Give the extent of all uninfected red blood cells.
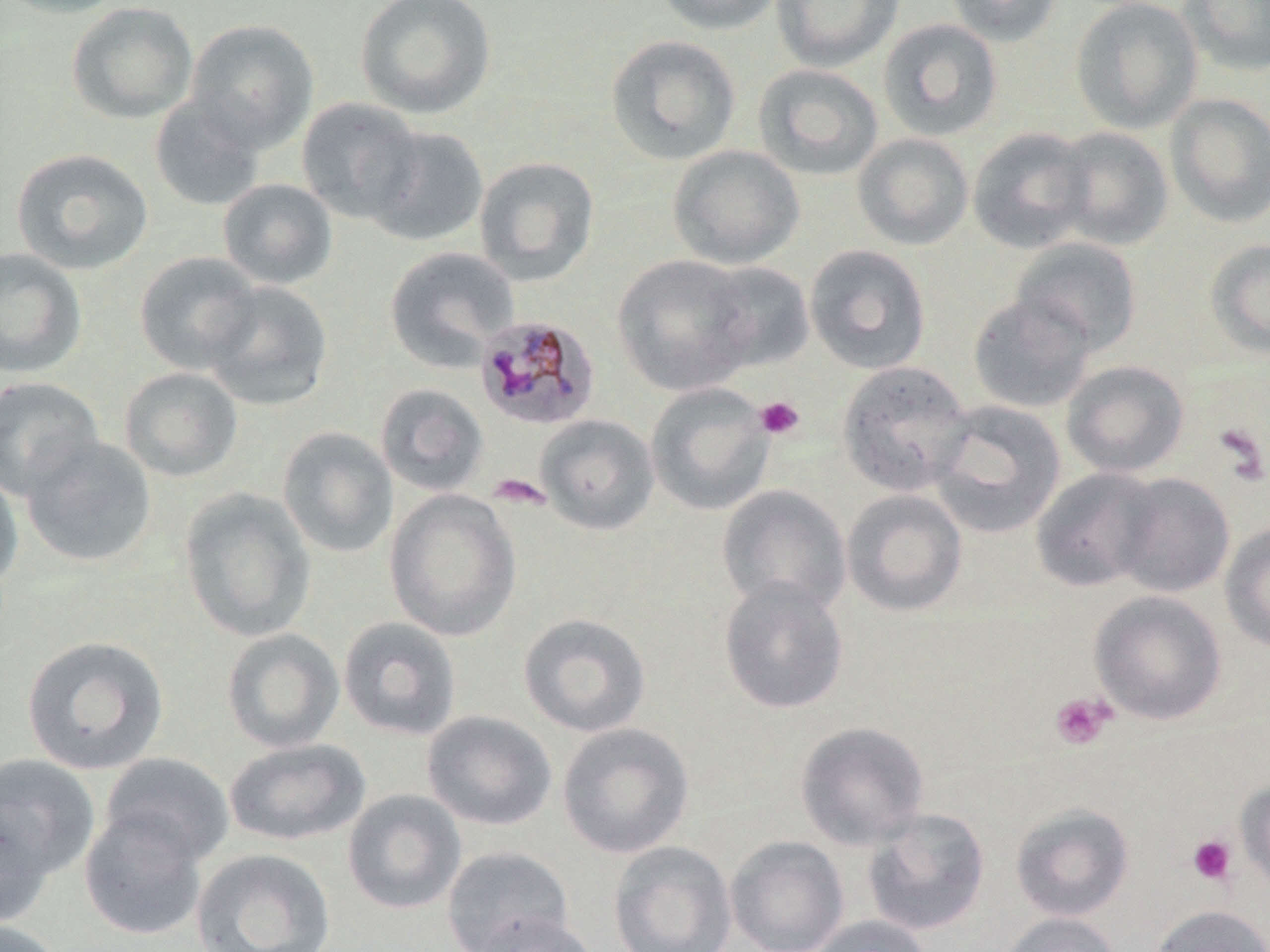
Approximate bounding boxes as (x1,y1)-(x2,y2) corner pairs in pixels.
Uninfected red blood cells: (0,0)-(131,19), (355,0)-(497,120), (654,0)-(785,35), (770,0)-(904,72), (944,0)-(1064,46), (1070,0)-(1203,134), (1180,0)-(1270,76), (66,2)-(198,125), (878,18)-(1003,142), (185,19)-(319,152), (605,34)-(742,166), (752,63)-(884,181), (1164,93)-(1270,228), (149,95)-(266,212), (296,97)-(424,224), (1055,109)-(1268,236), (364,126)-(489,247), (1051,126)-(1174,250), (967,127)-(1094,254), (852,133)-(974,251), (667,145)-(805,270), (11,148)-(154,275), (473,156)-(600,286), (217,178)-(338,289), (1010,237)-(1143,356), (1205,238)-(1270,359), (804,244)-(932,375), (0,246)-(88,379), (384,246)-(519,374), (134,251)-(261,373), (612,254)-(757,396), (700,261)-(816,373), (201,280)-(334,411), (968,292)-(1095,414), (837,360)-(974,496), (1061,360)-(1190,478), (119,367)-(243,482), (0,376)-(104,500), (375,383)-(489,496), (645,383)-(774,516), (926,400)-(1066,539), (535,414)-(660,535), (277,427)-(399,558), (21,435)-(157,568), (0,466)-(24,593), (1030,467)-(1162,593), (1111,472)-(1235,598), (717,485)-(852,616), (178,487)-(317,642), (385,489)-(521,642), (841,489)-(968,617), (1220,522)-(1270,653), (718,577)-(850,715), (1088,590)-(1228,725), (518,612)-(651,737), (338,616)-(462,740), (221,627)-(345,754), (21,635)-(169,776), (422,710)-(558,831), (794,720)-(930,850), (557,721)-(695,859), (224,737)-(370,846), (0,752)-(102,884), (99,753)-(234,867), (1235,779)-(1270,897), (342,789)-(467,915), (0,801)-(57,930), (1010,803)-(1134,921), (79,808)-(208,940), (862,808)-(990,936), (725,835)-(850,952), (608,841)-(737,952), (442,846)-(573,952), (190,847)-(336,952), (1149,903)-(1270,952), (471,912)-(601,952), (994,912)-(1123,952), (805,915)-(934,952), (0,919)-(66,952).

Plasmodium malariae-infected red blood cell locations: (474,314)-(601,431). Platelet locations: (754,396)-(805,440), (1212,423)-(1269,486), (487,474)-(551,510), (1049,692)-(1116,751), (1187,834)-(1238,886). Slide-level diagnosis: Plasmodium malariae. Thin blood film. May-Grünwald-Giemsa-stained preparation. 1000x magnification. Optical microscopy. Image is 1270×952 pixels. Single field of view.